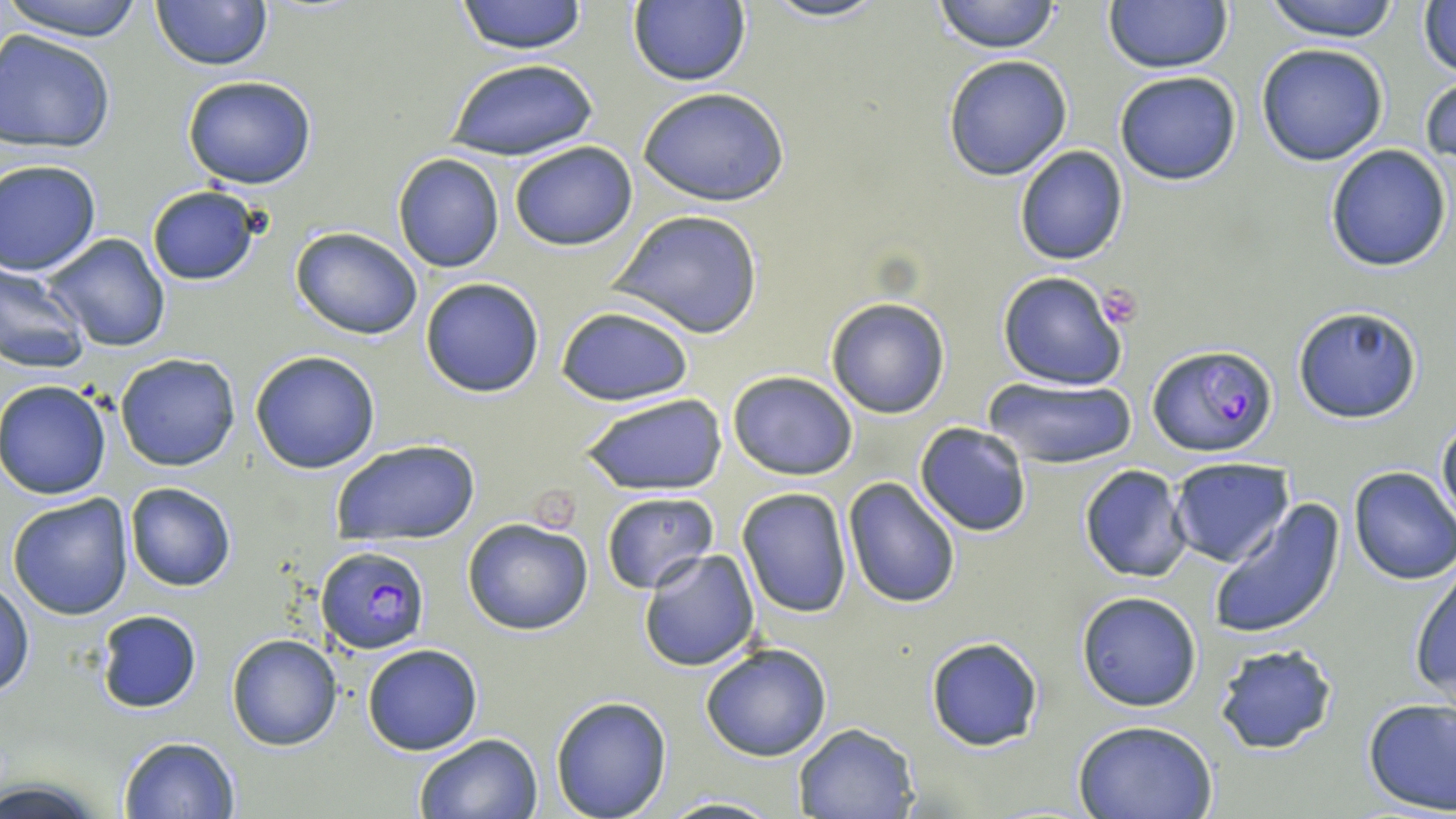
Approximate bounding boxes as (x1, y1, x2, y2) in pixels. Platelet locations: (1096, 284, 1144, 330). Plasmodium falciparum-infected red blood cell locations: (1145, 345, 1276, 458), (314, 547, 429, 654). Uninfected red blood cell locations: (4, 0, 149, 42), (151, 0, 274, 71), (456, 0, 586, 55), (626, 0, 751, 88), (760, 0, 890, 23), (931, 0, 1061, 54), (1261, 0, 1404, 41), (1104, 1, 1232, 73), (1418, 3, 1456, 81), (0, 28, 120, 151), (1256, 43, 1390, 166), (942, 55, 1073, 181), (448, 59, 597, 162), (1114, 71, 1241, 185), (1421, 72, 1456, 168), (182, 75, 318, 190), (639, 89, 789, 206), (508, 140, 638, 251), (1014, 144, 1129, 266), (1325, 145, 1453, 271), (391, 154, 505, 273), (1, 160, 102, 275), (145, 185, 261, 285), (611, 208, 764, 339), (291, 227, 424, 341), (41, 234, 170, 352), (0, 263, 88, 374), (996, 271, 1128, 392), (420, 276, 545, 397), (825, 297, 951, 418), (555, 305, 694, 406), (1292, 305, 1422, 424), (249, 349, 381, 474), (114, 353, 242, 471), (726, 369, 859, 479), (983, 374, 1137, 469), (1, 381, 114, 499), (580, 392, 726, 494), (1435, 410, 1456, 530), (915, 423, 1031, 536), (333, 438, 481, 544), (1168, 458, 1293, 568), (1079, 464, 1193, 583), (1347, 466, 1456, 584), (843, 479, 961, 609), (125, 482, 236, 592), (736, 488, 852, 617), (600, 492, 718, 593), (7, 493, 134, 620), (1208, 496, 1345, 641), (462, 519, 594, 636), (638, 549, 761, 671), (1410, 563, 1456, 706), (0, 581, 31, 699), (1075, 591, 1203, 711), (94, 608, 204, 712), (226, 633, 342, 751), (925, 637, 1045, 751), (702, 641, 832, 762), (361, 643, 484, 755), (1213, 643, 1337, 755), (550, 696, 672, 818), (1362, 698, 1456, 816), (1074, 718, 1220, 819), (792, 722, 918, 819), (413, 732, 544, 819), (117, 735, 239, 818), (656, 795, 788, 819). Slide-level diagnosis: Plasmodium falciparum. Single field of view. May-Grünwald-Giemsa-stained preparation. Image is 1456×819 pixels. Thin blood film. Light microscopy. 1000x magnification.